Classify this cell by malaria status.
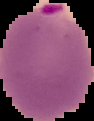

It is parasitized.

Image is 94×121 pixels. Segmented cell region on a black background. From a thin blood film.